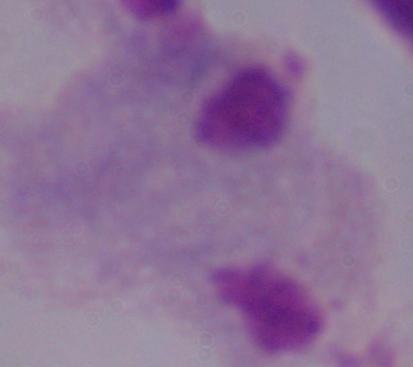
{
  "magnification": "1000x",
  "identification": "trichomonad",
  "modality": "photomicrograph"
}